Locate every blood parasite and identify its species.
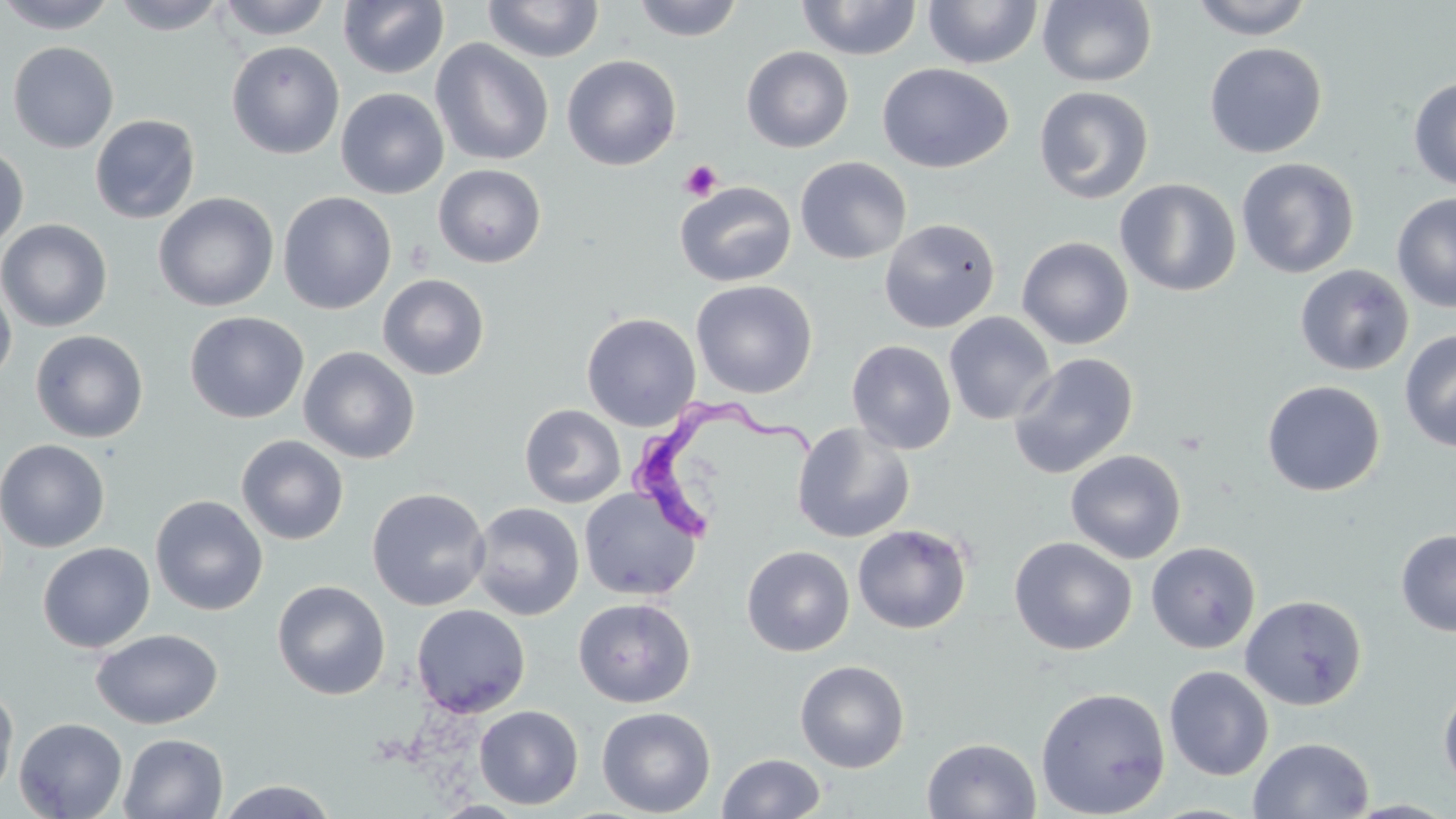

Approximate bounding boxes as (x1, y1, x2, y2) in pixels.
Trypanosoma brucei: (623, 396, 826, 545).
No Plasmodium falciparum, Plasmodium ovale, Plasmodium malariae, Plasmodium vivax, or Babesia divergens observed.

Platelet locations: (679, 160, 723, 201). Uninfected red blood cell locations: (0, 0, 119, 34), (111, 0, 230, 35), (216, 0, 333, 40), (338, 0, 450, 79), (632, 0, 744, 42), (797, 0, 922, 61), (1188, 0, 1315, 40), (482, 1, 604, 63), (922, 1, 1043, 69), (1037, 1, 1157, 87), (430, 38, 554, 166), (7, 41, 119, 153), (226, 41, 344, 159), (1204, 42, 1327, 158), (741, 46, 854, 153), (562, 54, 682, 171), (877, 63, 1014, 174), (1408, 76, 1456, 191), (1033, 85, 1155, 205), (335, 88, 449, 199), (89, 114, 201, 225), (0, 145, 29, 250), (795, 156, 912, 265), (1236, 158, 1359, 279), (433, 164, 547, 268), (1115, 178, 1241, 297), (674, 181, 796, 287), (278, 191, 397, 315), (153, 192, 278, 312), (1392, 192, 1456, 313), (0, 218, 113, 333), (879, 218, 1000, 333), (1016, 236, 1134, 349), (1294, 264, 1414, 376), (377, 273, 490, 380), (0, 279, 16, 388), (690, 279, 817, 398), (184, 311, 309, 424), (944, 311, 1056, 426), (581, 313, 701, 431), (30, 329, 149, 443), (1399, 330, 1456, 452), (846, 340, 957, 454), (298, 346, 421, 464), (1009, 352, 1138, 479), (1261, 380, 1386, 497), (520, 404, 626, 508), (791, 421, 915, 544), (236, 434, 349, 545), (0, 438, 110, 553), (1065, 449, 1187, 564), (367, 487, 491, 611), (579, 487, 702, 601), (150, 495, 268, 616), (469, 502, 584, 621), (852, 523, 973, 634), (1396, 529, 1456, 636), (1009, 536, 1137, 655), (1146, 541, 1261, 654), (37, 542, 155, 653), (741, 545, 854, 657), (272, 580, 391, 700), (1239, 594, 1367, 710), (573, 597, 696, 707), (412, 604, 530, 718), (91, 628, 223, 729), (794, 659, 910, 773), (1164, 666, 1274, 780), (0, 680, 18, 802), (1438, 681, 1456, 795), (1035, 686, 1171, 818), (474, 705, 584, 809), (596, 706, 716, 817), (13, 717, 128, 819), (118, 732, 228, 818), (1248, 736, 1374, 818), (922, 737, 1041, 818), (717, 752, 826, 818), (214, 779, 339, 818), (432, 800, 529, 818). Slide-level diagnosis: Trypanosoma brucei. 1000x magnification. Thin blood smear. May-Grünwald-Giemsa-stained preparation. Image is 1456×819 pixels. Light microscopy. One field of a larger specimen.